Name the blood parasite species.
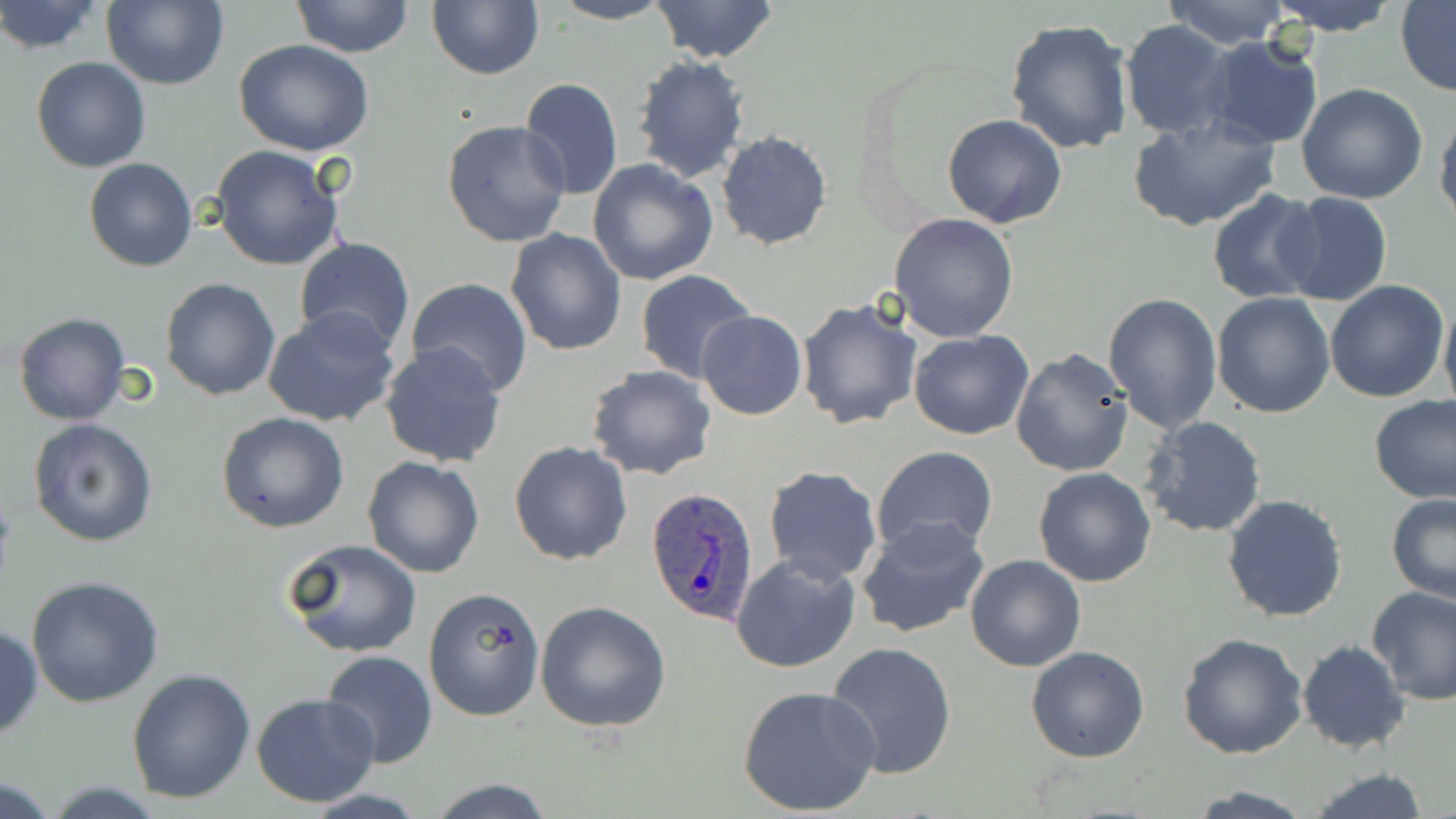

Plasmodium ovale.

Approximate bounding boxes as named x1/y1/x2/y2 corners in pixels. Plasmodium ovale-infected red blood cell locations: (x1=646, y1=486, x2=760, y2=626). Uninfected red blood cell locations: (x1=0, y1=0, x2=106, y2=56), (x1=291, y1=0, x2=413, y2=59), (x1=426, y1=0, x2=544, y2=80), (x1=548, y1=0, x2=677, y2=25), (x1=1160, y1=0, x2=1292, y2=49), (x1=1262, y1=0, x2=1404, y2=36), (x1=100, y1=1, x2=229, y2=90), (x1=652, y1=1, x2=777, y2=62), (x1=1395, y1=1, x2=1456, y2=93), (x1=1005, y1=18, x2=1136, y2=156), (x1=1119, y1=20, x2=1235, y2=140), (x1=1201, y1=36, x2=1325, y2=150), (x1=234, y1=39, x2=374, y2=156), (x1=630, y1=50, x2=751, y2=185), (x1=30, y1=57, x2=150, y2=173), (x1=519, y1=77, x2=623, y2=202), (x1=1296, y1=84, x2=1428, y2=205), (x1=1434, y1=107, x2=1456, y2=226), (x1=942, y1=114, x2=1067, y2=229), (x1=1127, y1=115, x2=1280, y2=232), (x1=441, y1=119, x2=572, y2=250), (x1=715, y1=131, x2=833, y2=249), (x1=212, y1=144, x2=345, y2=271), (x1=84, y1=158, x2=198, y2=271), (x1=587, y1=158, x2=718, y2=286), (x1=1206, y1=189, x2=1328, y2=307), (x1=1275, y1=192, x2=1393, y2=307), (x1=889, y1=213, x2=1019, y2=341), (x1=505, y1=227, x2=629, y2=356), (x1=294, y1=237, x2=415, y2=353), (x1=636, y1=269, x2=758, y2=385), (x1=162, y1=277, x2=280, y2=400), (x1=406, y1=277, x2=533, y2=398), (x1=1325, y1=280, x2=1451, y2=402), (x1=1101, y1=292, x2=1222, y2=434), (x1=1211, y1=293, x2=1336, y2=418), (x1=1439, y1=293, x2=1456, y2=416), (x1=796, y1=298, x2=924, y2=429), (x1=263, y1=306, x2=402, y2=428), (x1=697, y1=310, x2=807, y2=421), (x1=13, y1=312, x2=130, y2=427), (x1=909, y1=328, x2=1033, y2=441), (x1=380, y1=341, x2=509, y2=467), (x1=1012, y1=349, x2=1133, y2=477), (x1=585, y1=365, x2=716, y2=481), (x1=1371, y1=397, x2=1456, y2=506), (x1=216, y1=411, x2=350, y2=533), (x1=1140, y1=416, x2=1267, y2=539), (x1=27, y1=417, x2=159, y2=547), (x1=509, y1=442, x2=634, y2=566), (x1=871, y1=445, x2=996, y2=554), (x1=362, y1=455, x2=485, y2=578), (x1=762, y1=466, x2=884, y2=586), (x1=1033, y1=467, x2=1157, y2=586), (x1=1386, y1=492, x2=1456, y2=602), (x1=1222, y1=494, x2=1349, y2=623), (x1=856, y1=517, x2=989, y2=641), (x1=285, y1=538, x2=421, y2=658), (x1=731, y1=552, x2=861, y2=674), (x1=965, y1=556, x2=1085, y2=672), (x1=26, y1=575, x2=167, y2=707), (x1=1366, y1=584, x2=1456, y2=706), (x1=424, y1=587, x2=544, y2=721), (x1=535, y1=600, x2=671, y2=733), (x1=0, y1=624, x2=42, y2=739), (x1=1177, y1=632, x2=1308, y2=758), (x1=1296, y1=639, x2=1413, y2=753), (x1=826, y1=640, x2=958, y2=779), (x1=1026, y1=646, x2=1150, y2=764), (x1=319, y1=651, x2=437, y2=769), (x1=126, y1=668, x2=257, y2=803), (x1=738, y1=684, x2=881, y2=816), (x1=251, y1=693, x2=381, y2=807), (x1=1304, y1=766, x2=1433, y2=819), (x1=2, y1=776, x2=61, y2=818), (x1=424, y1=778, x2=559, y2=817), (x1=1181, y1=785, x2=1317, y2=818). One field of a larger specimen. May-Grünwald-Giemsa-stained preparation. Thin blood film. Optical microscopy. Image is 1456×819 pixels. Captured at 1000x magnification.